Give the extent of all Plasmodium ovale-infected red blood cells.
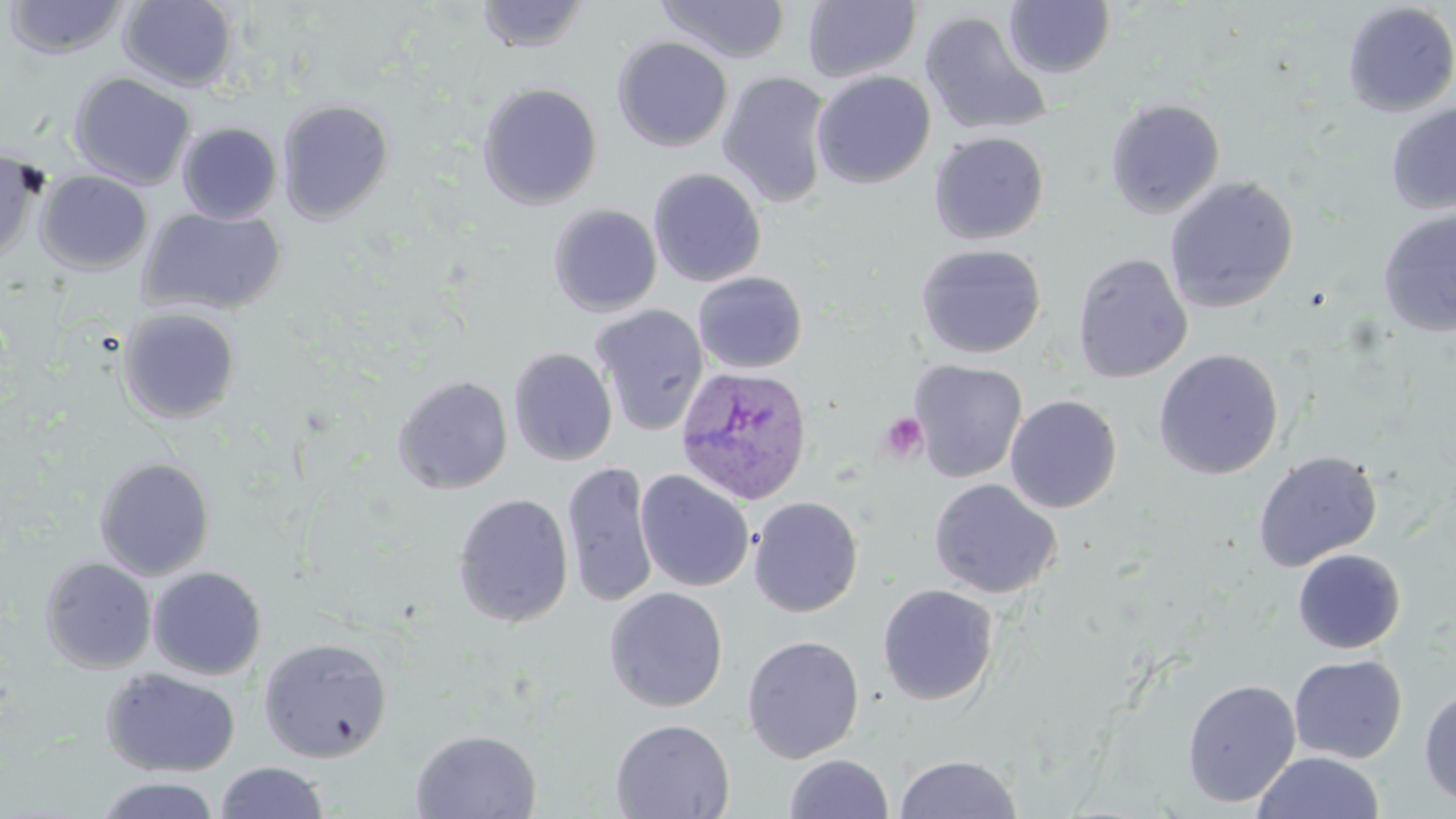
Approximate bounding boxes as (x1, y1, x2, y2) in pixels.
Plasmodium ovale-infected red blood cells: (675, 365, 812, 505).

Summary:
  - Platelet locations: (878, 412, 928, 462)
  - Uninfected red blood cell locations: (475, 0, 590, 53), (3, 1, 130, 60), (118, 1, 239, 91), (655, 1, 791, 64), (802, 1, 921, 82), (1003, 1, 1115, 78), (1342, 2, 1456, 117), (919, 10, 1052, 137), (612, 36, 733, 152), (812, 70, 936, 189), (717, 71, 834, 209), (69, 72, 196, 190), (478, 82, 603, 209), (1104, 97, 1225, 219), (277, 99, 394, 224), (1386, 102, 1456, 214), (177, 122, 283, 224), (929, 131, 1049, 244), (0, 147, 42, 262), (648, 167, 767, 287), (36, 170, 152, 274), (1164, 176, 1299, 313), (548, 204, 662, 316), (138, 207, 285, 317), (1377, 208, 1456, 337), (916, 244, 1046, 359), (1072, 252, 1193, 383), (693, 272, 807, 374), (590, 305, 709, 436), (118, 307, 242, 424), (508, 347, 618, 466), (1153, 349, 1284, 480), (909, 359, 1028, 483), (393, 373, 513, 494), (1005, 395, 1122, 513), (1253, 450, 1382, 571), (94, 457, 215, 580), (561, 462, 659, 608), (635, 470, 754, 592), (929, 478, 1062, 599), (453, 493, 574, 628), (748, 496, 863, 617), (1293, 549, 1406, 654), (40, 557, 156, 673), (148, 565, 266, 680), (877, 584, 998, 705), (604, 587, 729, 712), (741, 634, 865, 763), (258, 637, 392, 762), (1288, 654, 1407, 764), (102, 668, 241, 777), (1182, 679, 1301, 807), (1419, 687, 1456, 808), (610, 718, 735, 819), (410, 729, 541, 819), (1253, 750, 1384, 818), (784, 753, 893, 818), (893, 754, 1023, 818), (215, 761, 330, 819), (93, 775, 222, 819)
  - Slide-level diagnosis: Plasmodium ovale
  - Preparation: thin blood smear
  - Modality: light microscopy
  - Stain: May-Grünwald-Giemsa
  - Image size: 1456×819 pixels
  - Magnification: 1000x
  - Field of view: single